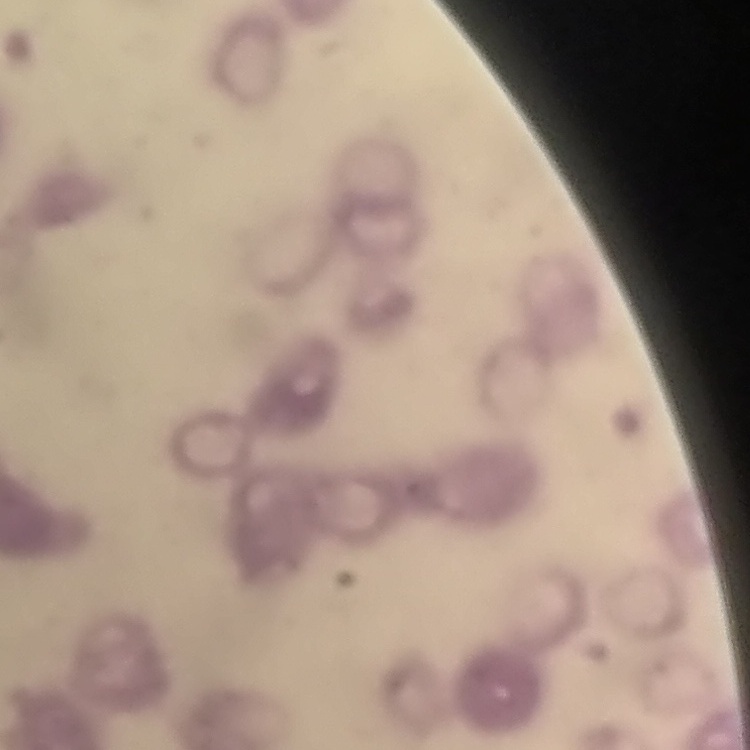
Summary:
  - Red blood cell morphology: rouleaux formation
  - Image type: one tile cut from a larger photomicrograph
  - Stain: Field's or Giemsa
  - Preparation: thin blood film